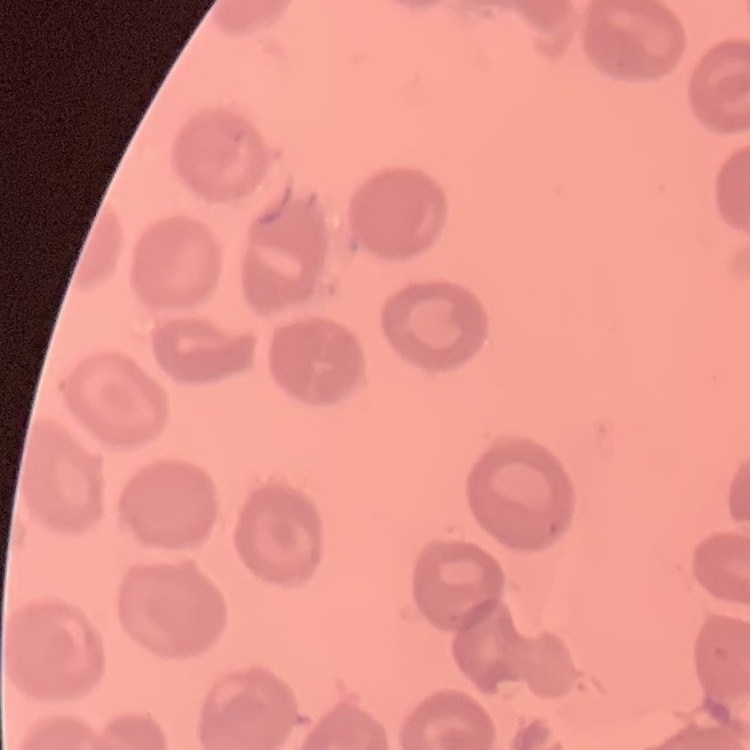
Summary:
  - Red blood cell morphology: no rouleaux formation
  - Preparation: thin blood smear
  - Stain: Field's or Giemsa
  - Image type: square crop of a larger photomicrograph